Identify the parasite.
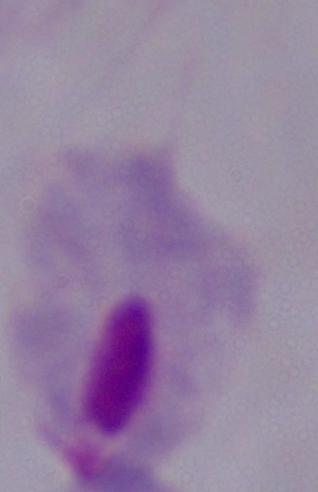

A trichomonad.

magnification = 1000x
modality = micrograph